Assess this cell for malaria.
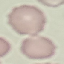
Uninfected.

Summary:
  - Capture: smartphone camera at the microscope eyepiece
  - Image type: cell patch, automatically extracted from a larger field of view and resized to 64 × 64 pixels
  - Stain: Giemsa
  - Preparation: thin blood smear